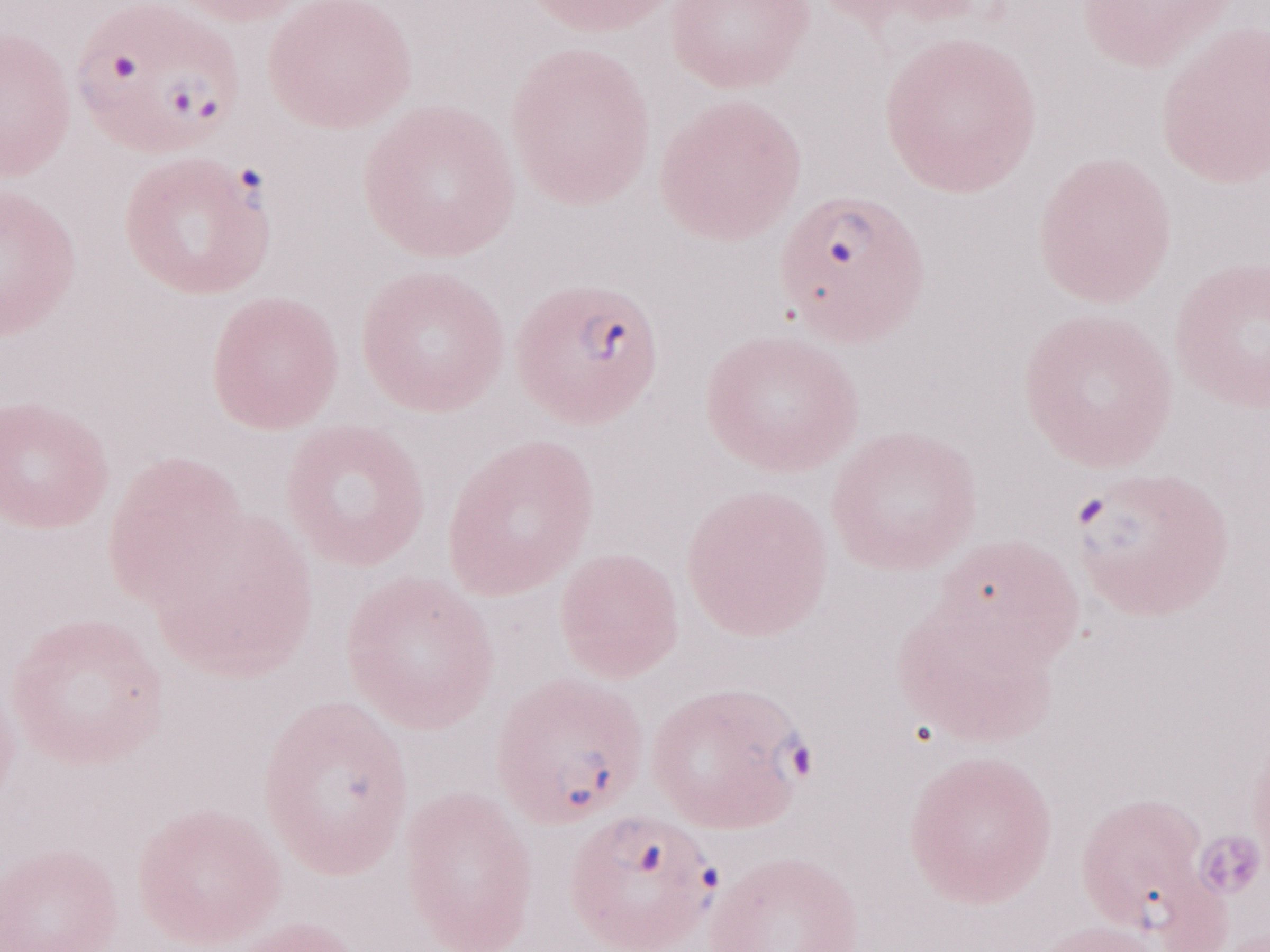

Olympus BX43 microscope and DP73 digital camera. Magnification: 1,000x. Image is 1270×952 pixels. Patient diagnosis: malaria infection. Thin blood film. May-Grünwald-Giemsa (MGG) stain. Single field of view.